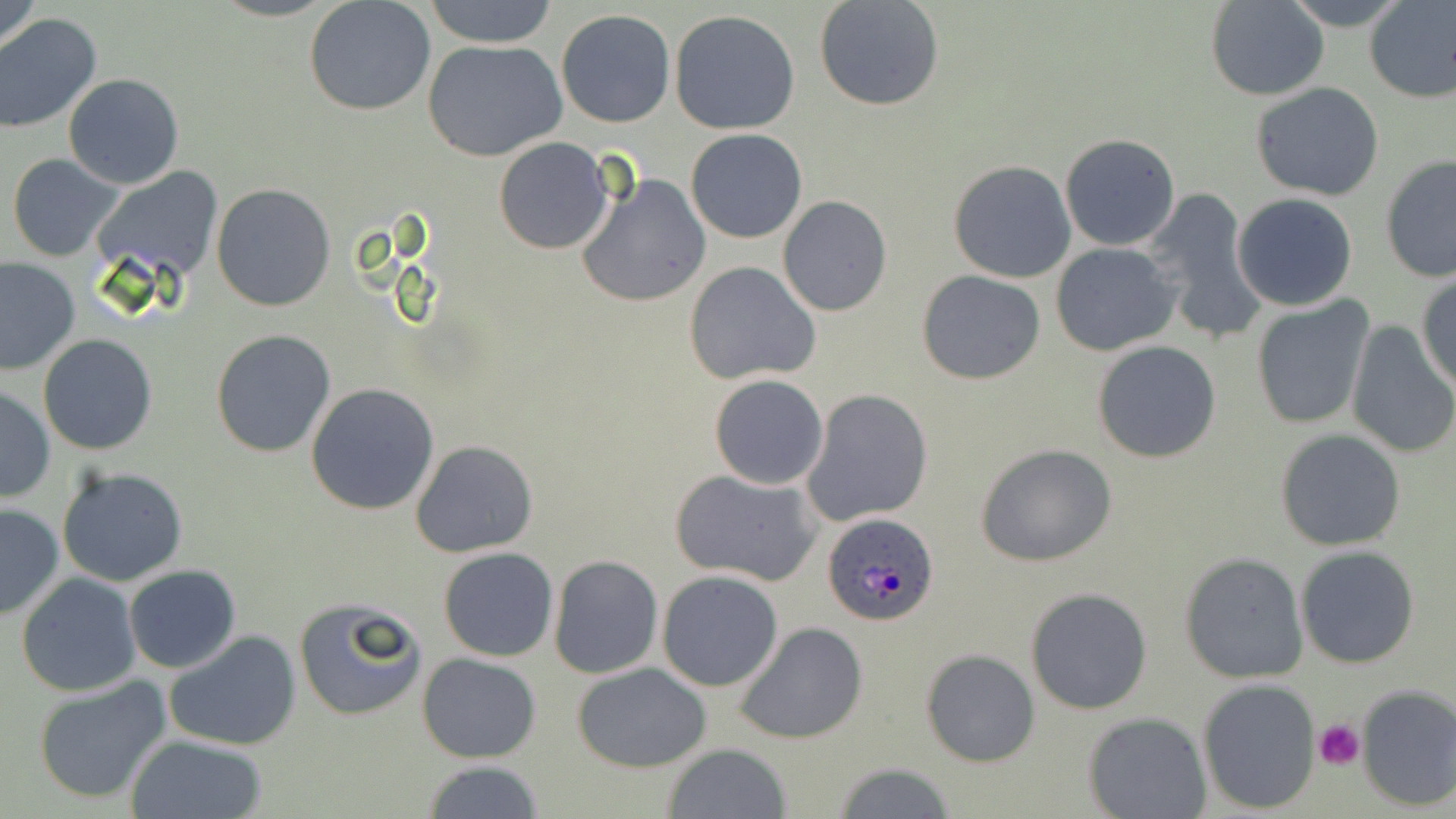

slide-level diagnosis = Plasmodium ovale
stain = May-Grünwald-Giemsa
field of view = one of a larger specimen
platelet locations = approximate bounding boxes as [x1, y1, x2, y2] in pixels: [1314, 719, 1365, 769]
preparation = thin blood smear
modality = optical microscopy
image size = 1456×819 pixels
magnification = 1000x
uninfected red blood cell locations = approximate bounding boxes as [x1, y1, x2, y2] in pixels: [0, 0, 47, 58], [304, 0, 437, 117], [424, 0, 560, 48], [1205, 0, 1330, 100], [1281, 0, 1408, 27], [1363, 0, 1456, 103], [814, 1, 946, 111], [555, 8, 676, 128], [669, 9, 800, 134], [0, 14, 102, 133], [423, 40, 568, 162], [62, 73, 185, 190], [1250, 82, 1386, 202], [685, 128, 808, 244], [1060, 134, 1182, 252], [494, 138, 612, 254], [6, 153, 125, 261], [1378, 156, 1455, 284], [948, 160, 1076, 283], [88, 167, 226, 283], [575, 172, 711, 309], [211, 183, 336, 312], [1141, 190, 1263, 342], [1232, 194, 1358, 311], [777, 196, 892, 317], [1050, 243, 1180, 356], [1, 256, 78, 376], [684, 261, 821, 386], [916, 270, 1046, 386], [1417, 274, 1456, 390], [1251, 298, 1374, 431], [1346, 322, 1456, 460], [210, 329, 337, 458], [38, 335, 158, 456], [1091, 339, 1222, 462], [709, 374, 829, 490], [0, 383, 55, 503], [306, 383, 440, 516], [802, 389, 934, 526], [1275, 429, 1405, 551], [410, 439, 539, 559], [976, 444, 1118, 567], [57, 467, 190, 587], [670, 470, 822, 588], [0, 503, 65, 621], [1296, 546, 1420, 667], [439, 547, 559, 661], [1180, 552, 1309, 682], [548, 554, 662, 679], [124, 565, 241, 674], [657, 571, 784, 691], [17, 573, 141, 697], [1025, 586, 1153, 716], [293, 595, 429, 721], [734, 621, 869, 745], [165, 631, 302, 752], [920, 650, 1039, 767], [417, 652, 542, 763], [572, 662, 711, 772], [30, 677, 174, 807], [1197, 678, 1323, 814], [1355, 684, 1456, 813], [1084, 712, 1212, 819], [125, 735, 267, 819], [660, 744, 793, 819], [422, 760, 546, 818], [830, 761, 958, 817]
Plasmodium ovale-infected red blood cell locations = approximate bounding boxes as [x1, y1, x2, y2] in pixels: [820, 512, 939, 626]